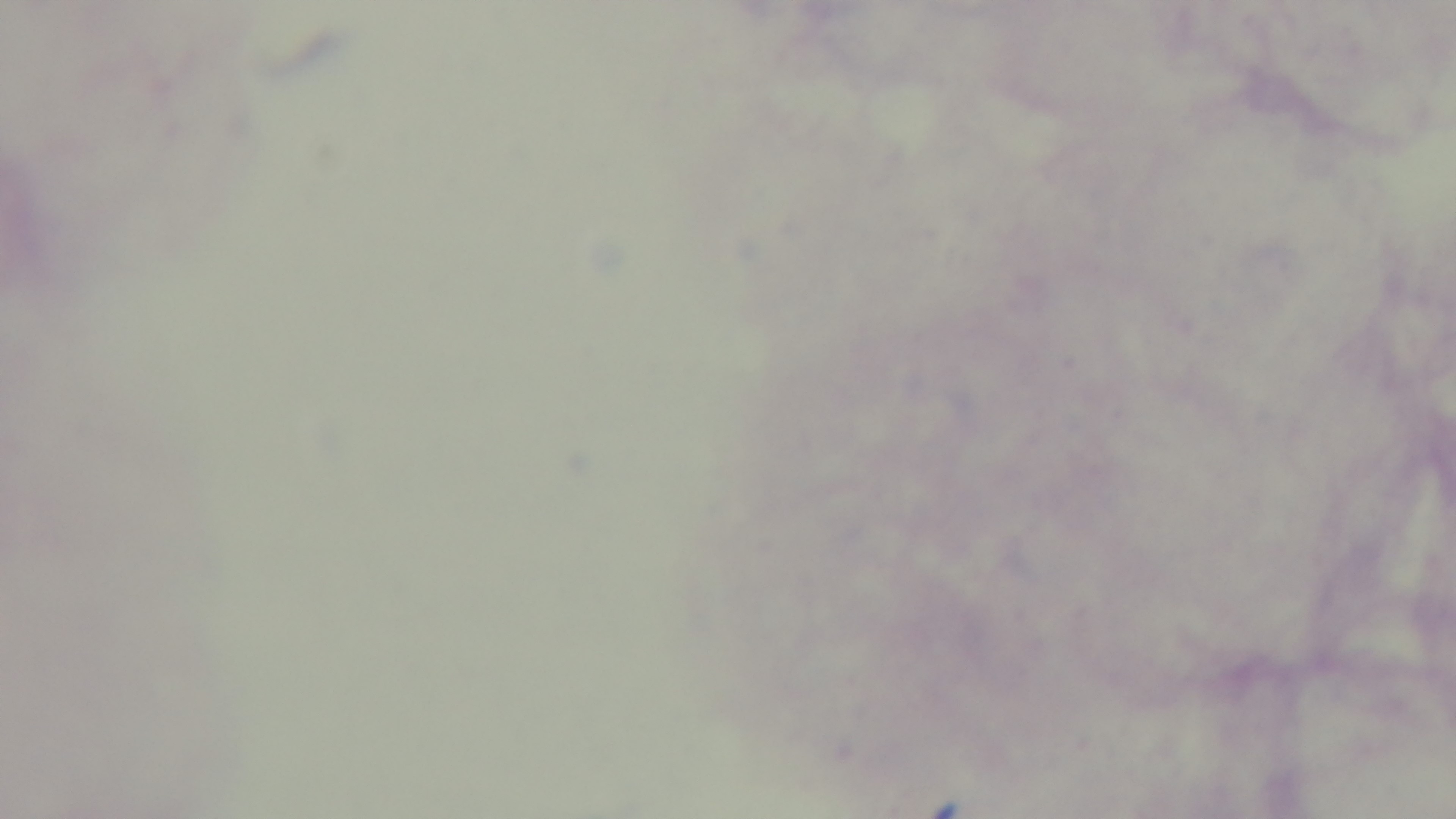

Summary:
  - Modality: light microscopy
  - Stain: Giemsa
  - Malaria status: negative
  - Preparation: thick
  - Objective: 100x oil immersion
  - Field of view: one from the slide
  - Capture: mounted 4K digital camera